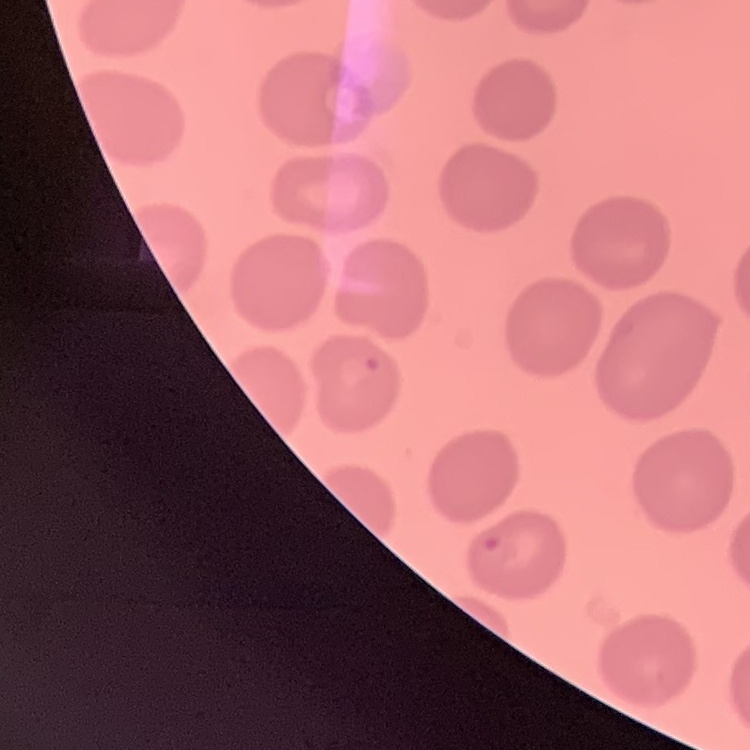

{
  "erythrocyte_morphology": "no rouleaux formation",
  "preparation": "thin blood film",
  "image_type": "one tile cut from a larger photomicrograph",
  "stain": "Field's or Giemsa"
}